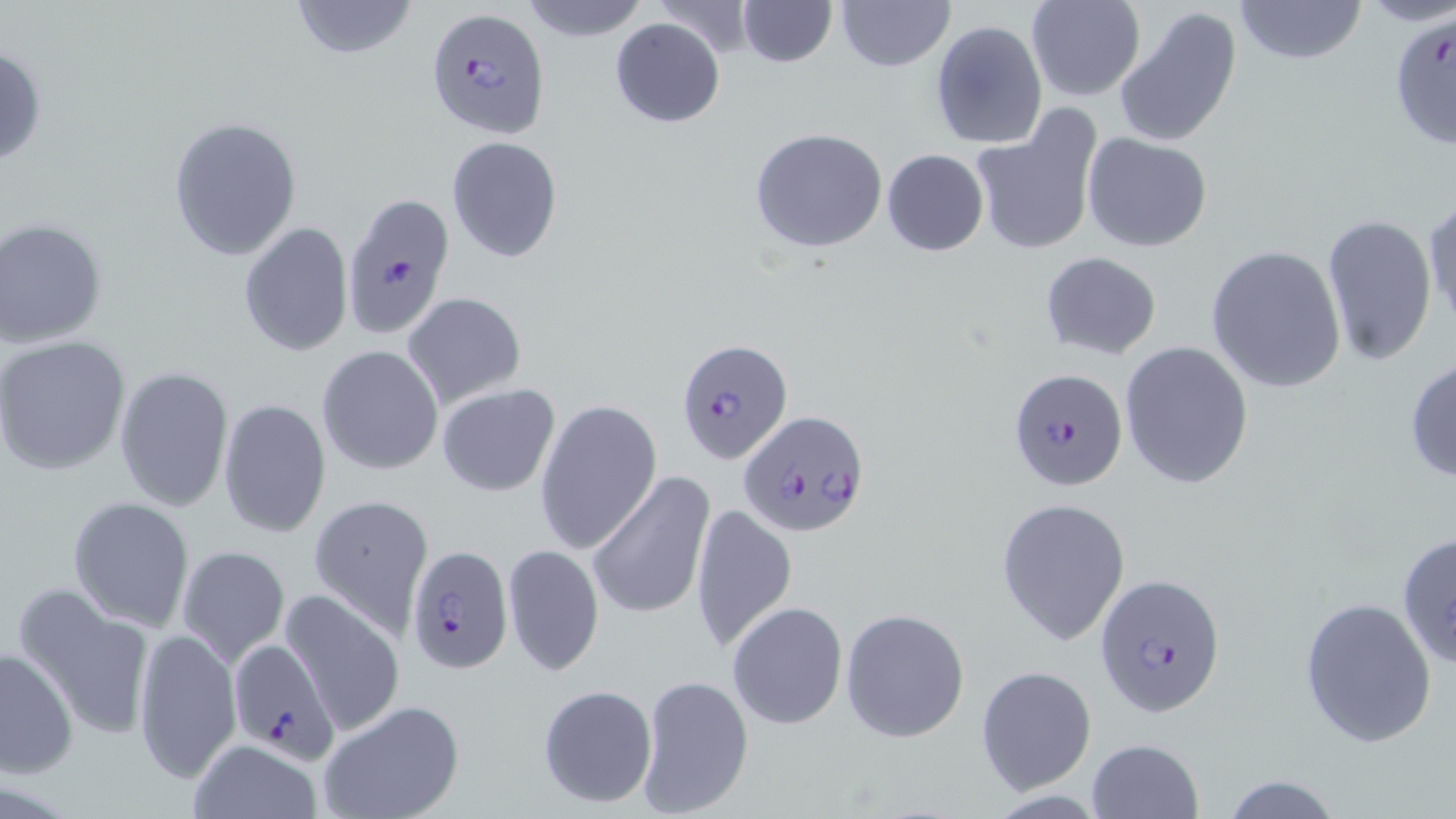

slide_level_diagnosis: Plasmodium falciparum
uninfected_red_blood_cell_locations: 'approximate bounding boxes as [x1, y1, x2, y2] in pixels: [289, 0, 421, 59], [518, 0, 649, 41], [653, 0, 759, 60], [736, 0, 836, 67], [835, 0, 955, 71], [1026, 0, 1145, 101], [1235, 0, 1366, 66], [1113, 7, 1242, 146], [610, 17, 726, 127], [930, 20, 1047, 152], [0, 43, 48, 169], [969, 112, 1102, 256], [168, 115, 302, 260], [749, 128, 888, 253], [1082, 131, 1212, 251], [446, 136, 563, 262], [882, 149, 989, 256], [1424, 197, 1455, 336], [1320, 215, 1437, 369], [1, 217, 107, 346], [239, 221, 354, 359], [1205, 245, 1348, 394], [1040, 251, 1163, 360], [401, 292, 526, 408], [0, 337, 131, 473], [1119, 341, 1254, 490], [317, 345, 443, 474], [1404, 355, 1456, 485], [114, 365, 233, 511], [436, 384, 561, 496], [534, 397, 661, 556], [218, 398, 333, 538], [586, 473, 713, 620], [308, 493, 435, 635], [67, 495, 195, 632], [995, 496, 1132, 644], [689, 503, 798, 653], [1395, 530, 1456, 669], [177, 544, 289, 666], [502, 544, 604, 677], [13, 583, 156, 742], [281, 591, 405, 737], [1299, 597, 1438, 748], [727, 601, 848, 730], [840, 607, 969, 743], [133, 626, 241, 783], [1, 648, 77, 777], [975, 665, 1097, 796], [635, 673, 754, 819], [536, 682, 658, 809], [318, 699, 464, 819], [187, 738, 324, 819], [1086, 738, 1204, 819], [1220, 774, 1345, 818]'
modality: light microscopy
stain: May-Grünwald-Giemsa
field_of_view: one of a larger specimen
image_size: 1456×819 pixels
magnification: 1000x
plasmodium_falciparum_infected_red_blood_cell_locations: 'approximate bounding boxes as [x1, y1, x2, y2] in pixels: [427, 8, 550, 136], [337, 198, 452, 346], [675, 338, 793, 467], [1008, 368, 1127, 490], [737, 410, 872, 541], [405, 545, 511, 674], [1095, 573, 1226, 719], [228, 639, 340, 762]'
preparation: thin blood film